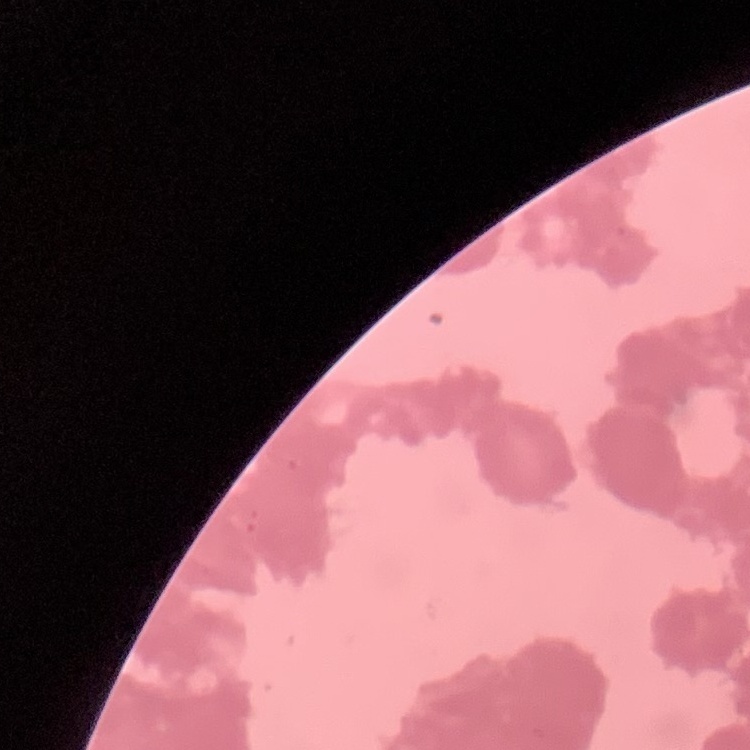

The red blood cells exhibit rouleaux formation. Field's or Giemsa stain. Thin blood smear. One tile cut from a larger photomicrograph.